Outline each blood parasite and name the species.
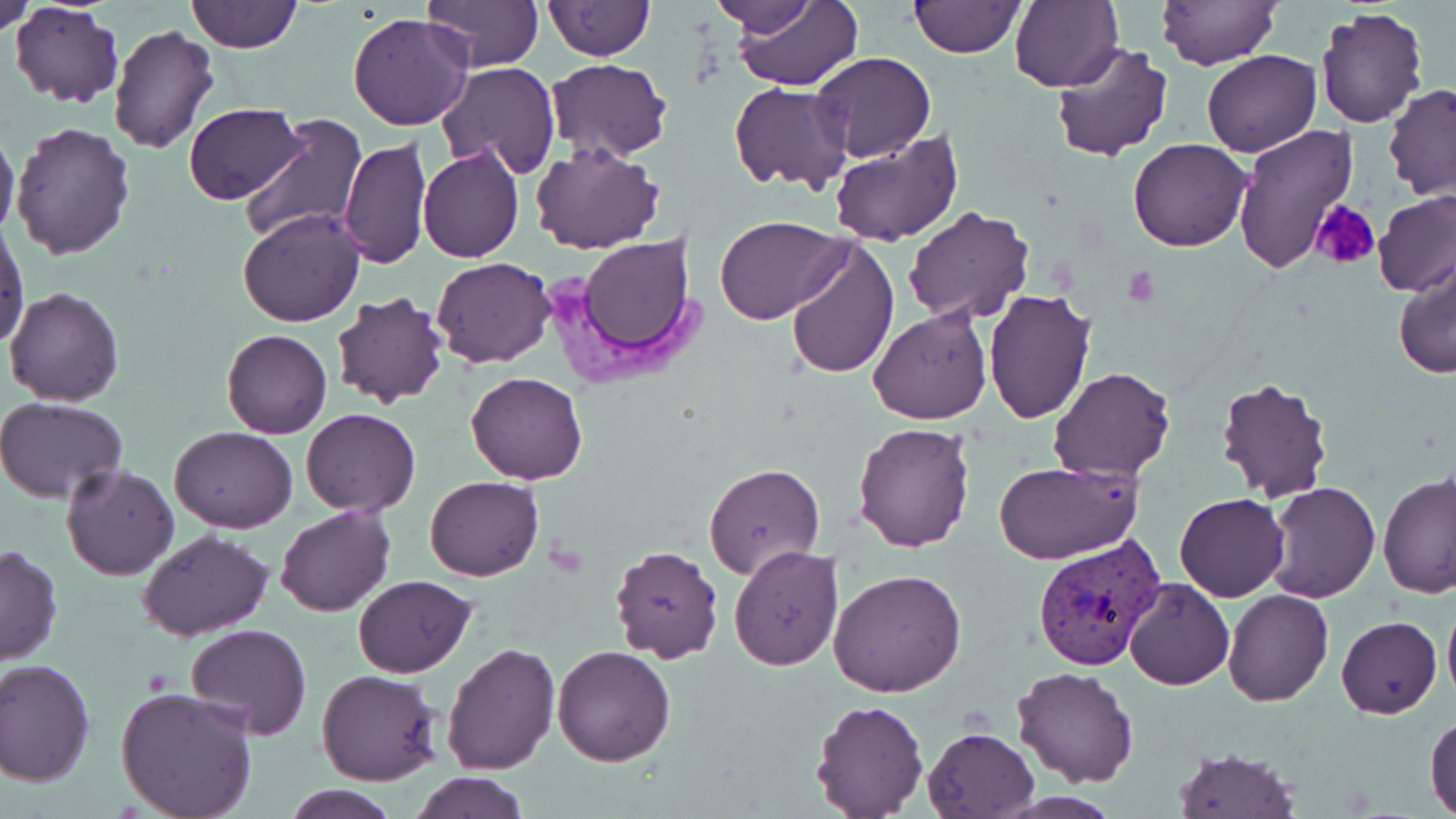

Approximate bounding boxes as [x1, y1, x2, y2] in pixels.
Plasmodium vivax-infected red blood cells: [1030, 534, 1172, 668].
No Plasmodium falciparum, Plasmodium ovale, Plasmodium malariae, Babesia divergens, or Trypanosoma brucei observed.

Platelet locations: [1310, 201, 1380, 268], [1121, 266, 1161, 307]. Uninfected red blood cell locations: [1, 0, 37, 36], [10, 0, 124, 108], [187, 0, 302, 53], [425, 0, 541, 72], [543, 0, 653, 60], [704, 0, 829, 42], [727, 0, 863, 91], [1010, 0, 1124, 94], [1157, 0, 1278, 70], [908, 1, 1025, 57], [1314, 7, 1429, 130], [348, 12, 473, 131], [107, 23, 222, 157], [1050, 42, 1174, 164], [1201, 50, 1321, 158], [811, 52, 937, 164], [546, 58, 673, 162], [437, 62, 561, 180], [729, 83, 855, 195], [1382, 84, 1456, 199], [183, 102, 304, 203], [238, 111, 367, 245], [12, 121, 135, 260], [1231, 123, 1358, 274], [0, 125, 19, 242], [829, 130, 964, 245], [340, 138, 432, 269], [1128, 139, 1251, 253], [530, 143, 663, 255], [416, 144, 524, 263], [1373, 190, 1456, 296], [903, 205, 1035, 325], [238, 208, 366, 328], [714, 216, 849, 324], [1, 223, 28, 349], [561, 234, 701, 373], [786, 240, 898, 378], [431, 257, 557, 368], [1392, 259, 1456, 379], [5, 286, 125, 406], [982, 289, 1096, 424], [331, 291, 447, 409], [868, 308, 993, 425], [221, 329, 332, 440], [1049, 366, 1177, 482], [466, 371, 588, 486], [1214, 374, 1335, 501], [1, 399, 128, 504], [300, 408, 421, 516], [853, 421, 976, 552], [170, 425, 297, 533], [994, 461, 1141, 567], [703, 463, 825, 579], [61, 464, 180, 582], [1379, 473, 1456, 599], [424, 476, 543, 581], [1264, 482, 1382, 603], [1175, 493, 1288, 602], [276, 505, 395, 618], [136, 530, 275, 641], [0, 544, 63, 666], [609, 544, 725, 663], [728, 547, 844, 670], [828, 569, 967, 697], [352, 575, 476, 676], [1123, 578, 1234, 690], [1223, 590, 1333, 706], [1442, 596, 1456, 705], [1337, 615, 1441, 719], [185, 625, 312, 741], [441, 642, 560, 776], [551, 644, 676, 767], [1, 660, 96, 787], [1012, 665, 1140, 787], [318, 670, 441, 785], [114, 686, 260, 819], [808, 699, 928, 817], [1426, 713, 1456, 816], [924, 728, 1040, 818], [1172, 748, 1298, 819], [411, 770, 529, 819], [281, 783, 402, 819]. Slide-level diagnosis: Plasmodium vivax. Thin blood smear. 1000x magnification. Image is 1456×819 pixels. Single field of view. Optical microscopy. May-Grünwald-Giemsa-stained preparation.